State which parasite is depicted.
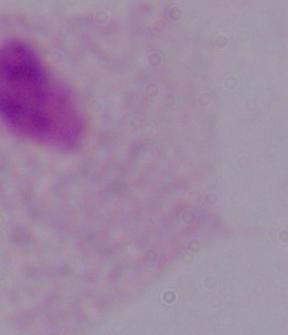
This is a trichomonad.

{
  "magnification": "1000x",
  "modality": "micrograph"
}